Locate every blood parasite and identify its species.
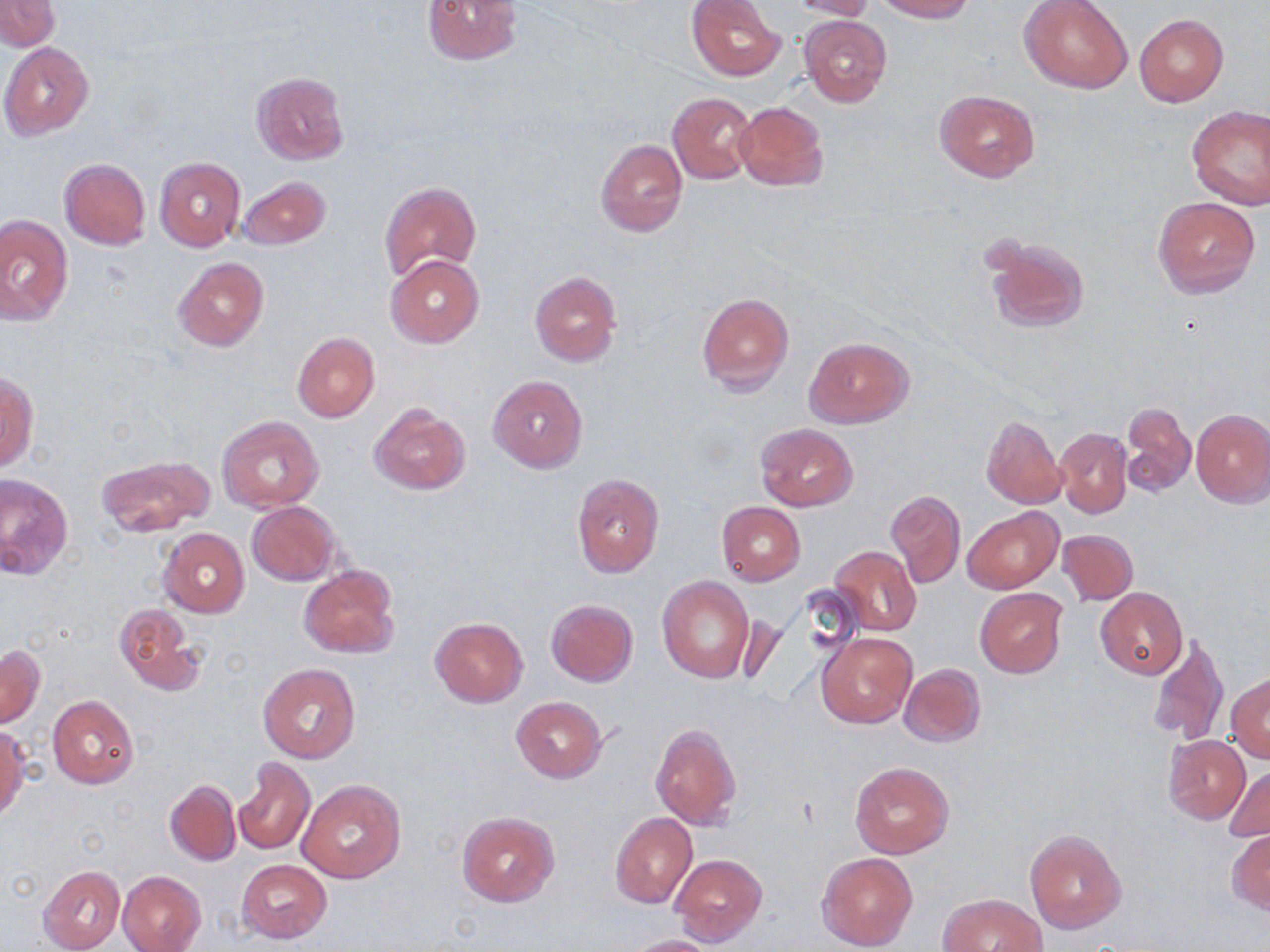

No blood parasites seen.

Summary:
  - Coordinate format: approximate bounding boxes as named x1/y1/x2/y2 corners in pixels
  - Uninfected red blood cell locations: (x1=423, y1=0, x2=524, y2=64), (x1=686, y1=0, x2=785, y2=81), (x1=786, y1=0, x2=877, y2=20), (x1=875, y1=0, x2=975, y2=22), (x1=1020, y1=0, x2=1133, y2=94), (x1=1, y1=1, x2=59, y2=50), (x1=1135, y1=14, x2=1228, y2=105), (x1=799, y1=15, x2=892, y2=107), (x1=1, y1=42, x2=94, y2=140), (x1=252, y1=72, x2=348, y2=166), (x1=934, y1=89, x2=1041, y2=183), (x1=667, y1=92, x2=757, y2=184), (x1=733, y1=101, x2=829, y2=192), (x1=1187, y1=106, x2=1270, y2=209), (x1=596, y1=139, x2=686, y2=236), (x1=155, y1=157, x2=245, y2=252), (x1=59, y1=159, x2=151, y2=250), (x1=236, y1=176, x2=330, y2=249), (x1=379, y1=181, x2=482, y2=282), (x1=1154, y1=197, x2=1259, y2=299), (x1=1, y1=215, x2=72, y2=326), (x1=985, y1=235, x2=1091, y2=335), (x1=386, y1=255, x2=485, y2=348), (x1=172, y1=257, x2=268, y2=352), (x1=530, y1=271, x2=621, y2=369), (x1=696, y1=294, x2=794, y2=395), (x1=293, y1=332, x2=379, y2=422), (x1=804, y1=336, x2=914, y2=429), (x1=1, y1=371, x2=37, y2=472), (x1=488, y1=374, x2=587, y2=472), (x1=1121, y1=402, x2=1196, y2=497), (x1=368, y1=404, x2=470, y2=495), (x1=1192, y1=408, x2=1270, y2=507), (x1=980, y1=415, x2=1065, y2=510), (x1=1056, y1=416, x2=1193, y2=506), (x1=218, y1=417, x2=324, y2=513), (x1=756, y1=423, x2=857, y2=511), (x1=1054, y1=428, x2=1131, y2=518), (x1=96, y1=454, x2=215, y2=537), (x1=572, y1=474, x2=664, y2=578), (x1=0, y1=476, x2=73, y2=580), (x1=888, y1=490, x2=966, y2=588), (x1=247, y1=501, x2=341, y2=586), (x1=717, y1=502, x2=805, y2=585), (x1=964, y1=506, x2=1061, y2=593), (x1=159, y1=528, x2=249, y2=617), (x1=1059, y1=530, x2=1139, y2=605), (x1=830, y1=544, x2=921, y2=637), (x1=298, y1=565, x2=399, y2=660), (x1=657, y1=576, x2=755, y2=682), (x1=1095, y1=587, x2=1187, y2=680), (x1=974, y1=589, x2=1067, y2=677), (x1=545, y1=599, x2=638, y2=686), (x1=114, y1=603, x2=204, y2=698), (x1=430, y1=618, x2=529, y2=708), (x1=816, y1=631, x2=917, y2=728), (x1=1146, y1=634, x2=1229, y2=747), (x1=1, y1=645, x2=44, y2=728), (x1=259, y1=663, x2=362, y2=763), (x1=899, y1=663, x2=986, y2=747), (x1=1227, y1=673, x2=1270, y2=762), (x1=48, y1=695, x2=139, y2=789), (x1=511, y1=696, x2=607, y2=784), (x1=650, y1=723, x2=741, y2=831), (x1=0, y1=726, x2=28, y2=820), (x1=1162, y1=735, x2=1250, y2=825), (x1=233, y1=757, x2=315, y2=856), (x1=849, y1=761, x2=953, y2=859), (x1=1225, y1=765, x2=1270, y2=844), (x1=164, y1=779, x2=240, y2=866), (x1=298, y1=779, x2=406, y2=884), (x1=457, y1=811, x2=559, y2=907), (x1=609, y1=812, x2=696, y2=909), (x1=1024, y1=829, x2=1127, y2=934), (x1=1227, y1=830, x2=1269, y2=913), (x1=816, y1=852, x2=919, y2=950), (x1=670, y1=853, x2=767, y2=947), (x1=236, y1=859, x2=331, y2=943), (x1=39, y1=865, x2=125, y2=951), (x1=119, y1=870, x2=207, y2=951), (x1=938, y1=893, x2=1046, y2=952), (x1=625, y1=935, x2=724, y2=952)
  - Slide-level diagnosis: negative for blood parasites
  - Magnification: 1000x
  - Modality: optical microscopy
  - Field of view: one of a larger specimen
  - Image size: 1270×952 pixels
  - Stain: May-Grünwald-Giemsa
  - Preparation: thin blood film